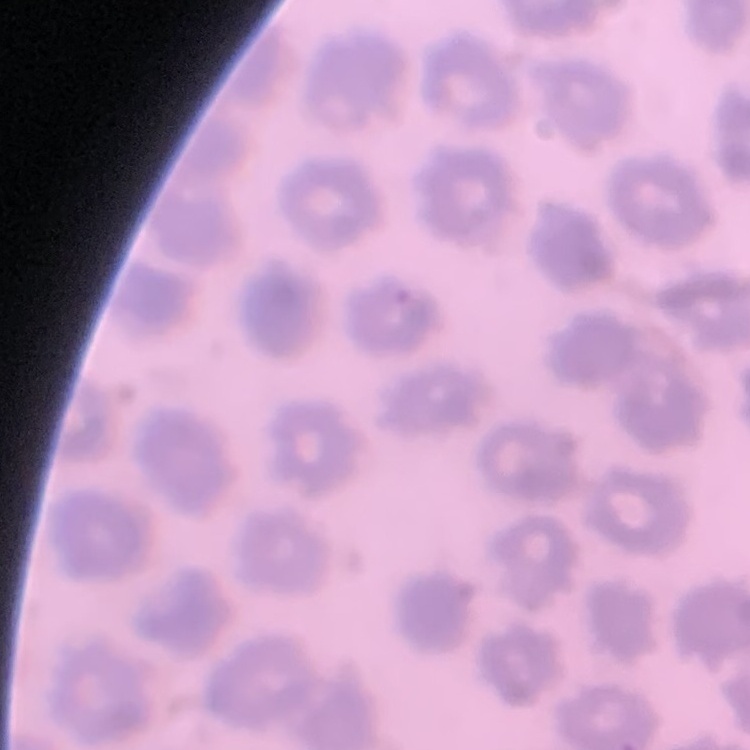
red blood cell morphology = no rouleaux formation
image type = square crop of a larger photomicrograph
stain = Field's or Giemsa
preparation = thin blood film